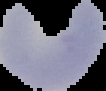

image size = 106×91 pixels
result = negative for malaria parasites
preparation = thin blood smear
image type = segmented cell region with the area outside set to black